Classify this cell by malaria status.
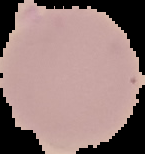

It is uninfected.

Summary:
  - Image size: 145×154 pixels
  - Preparation: thin blood smear
  - Image type: cell region segmented out of the field of view; surrounding area masked to black